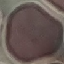
malaria_status: uninfected
capture: smartphone through the microscope eyepiece
stain: Giemsa
image_type: cell patch, automatically extracted from a larger field of view and resized to 64 × 64 pixels
preparation: thin smear